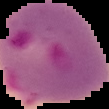
Summary:
  - Malaria status: parasitized
  - Image size: 109×109 pixels
  - Preparation: thin blood film
  - Image type: segmented cell region on a black background